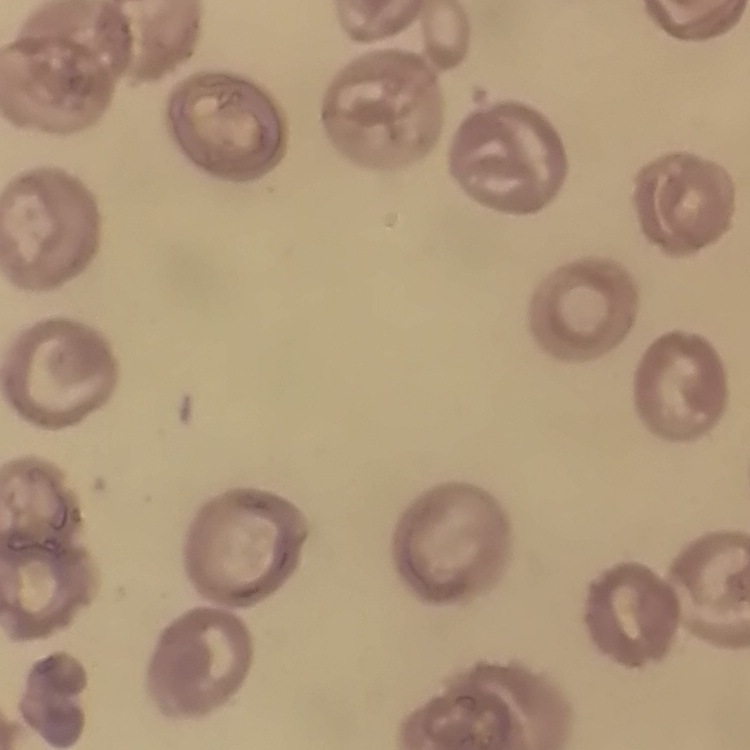

erythrocyte morphology = no rouleaux formation
preparation = thin peripheral smear
image type = square crop of a larger photomicrograph
stain = Field's or Giemsa